Point out each leukocyte.
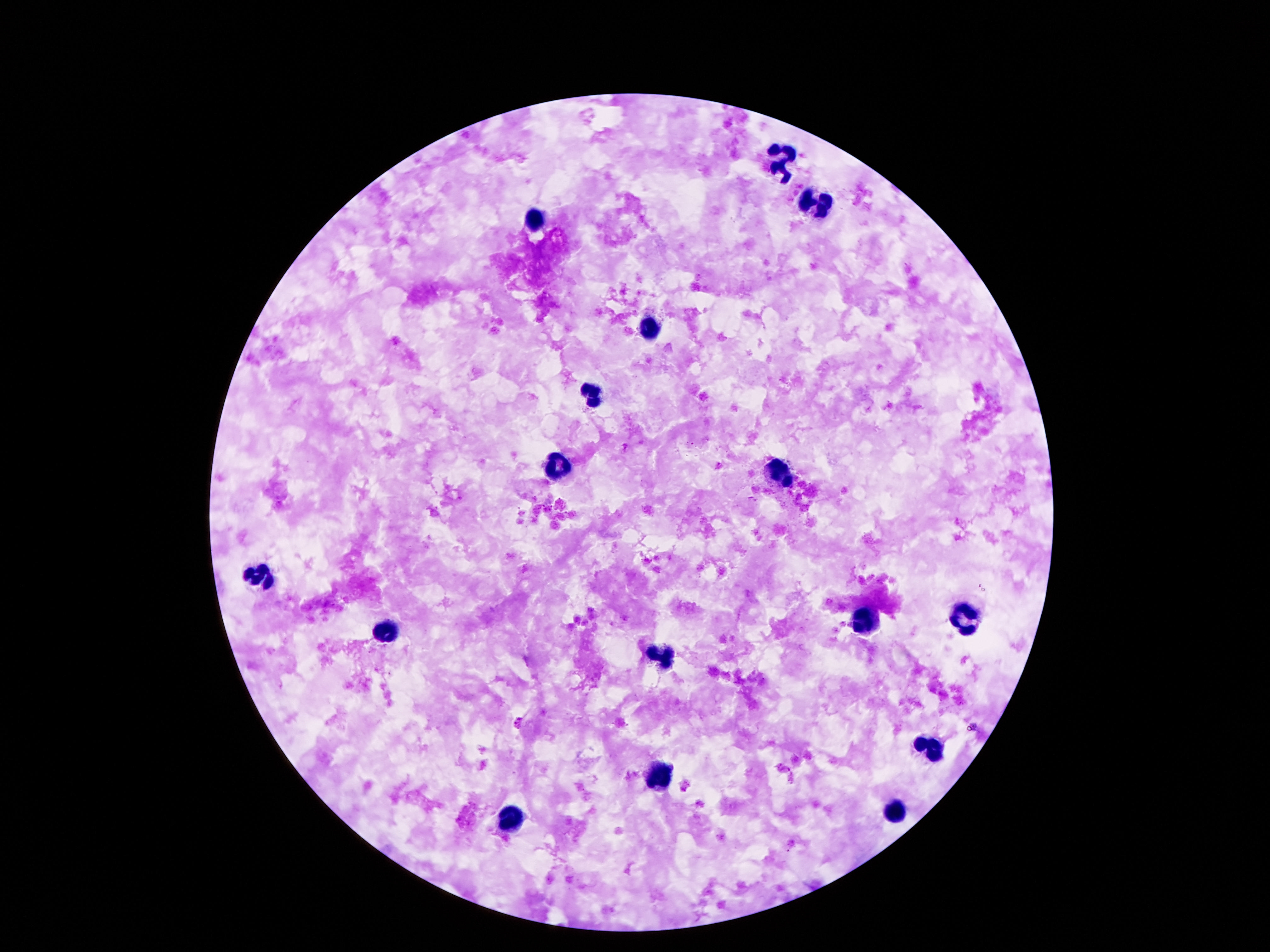
Approximate centers as (x, y) in pixels.
Leukocytes: (780, 163), (816, 205), (535, 222), (646, 330), (591, 394), (557, 470), (778, 476), (257, 579), (963, 620), (867, 624), (382, 634), (663, 655), (927, 747), (658, 779), (893, 810), (509, 817).

field_of_view: single
patient_malaria_status: uninfected
capture: smartphone camera through the microscope eyepiece
magnification: 100x
preparation: thick peripheral-blood smear
stain: Giemsa
image_size: 1270×952 pixels